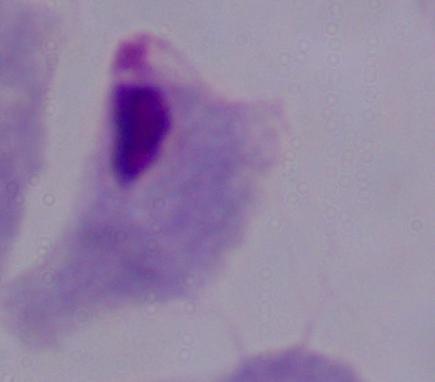
modality = micrograph
identification = trichomonad
magnification = 1000x